Name the cell type shown.
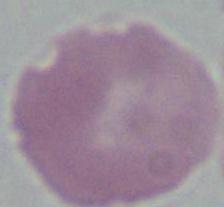

This is an erythrocyte.

Photomicrograph. Captured at 1000x magnification.